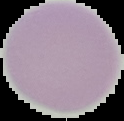

image type = segmented cell region on a black background
malaria status = uninfected
image size = 124×121 pixels
preparation = thin blood film